Identify the parasite.
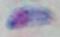
This is Toxoplasma gondii.

Summary:
  - Magnification: 1000x
  - Modality: micrograph